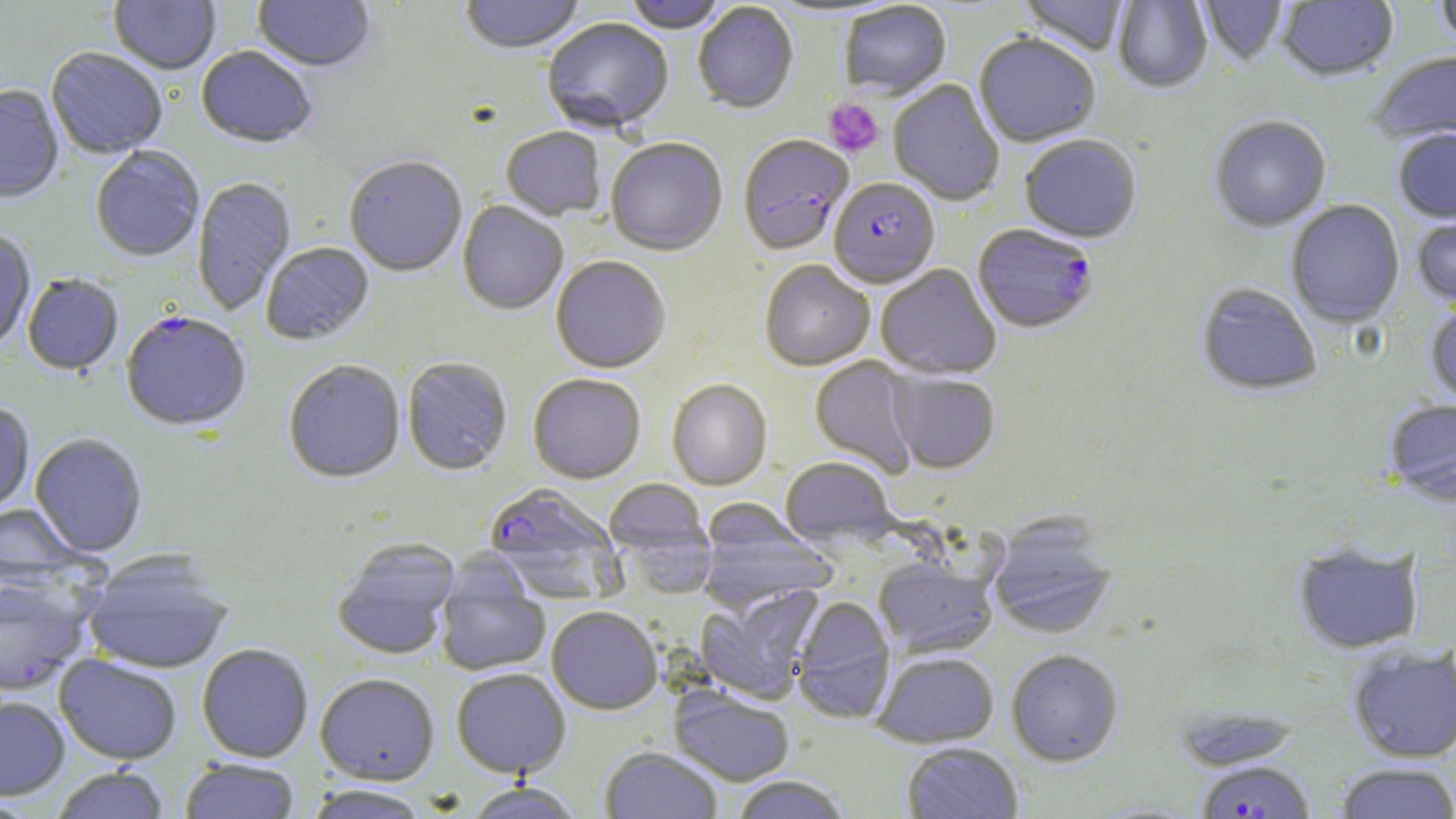
slide-level diagnosis = Plasmodium falciparum
preparation = thin blood smear
modality = light microscopy
field of view = one of a larger specimen
stain = May-Grünwald-Giemsa
image size = 1456×819 pixels
Plasmodium falciparum-infected red blood cell locations = approximate bounding boxes as [x1, y1, x2, y2] in pixels: [737, 136, 853, 256], [829, 179, 940, 290], [973, 225, 1098, 336], [121, 313, 251, 433], [484, 483, 622, 602], [1195, 759, 1317, 819]
platelet locations = approximate bounding boxes as [x1, y1, x2, y2] in pixels: [824, 98, 884, 158]
uninfected red blood cell locations = approximate bounding boxes as [x1, y1, x2, y2] in pixels: [109, 0, 221, 75], [253, 0, 375, 75], [460, 0, 585, 57], [623, 0, 728, 35], [1018, 0, 1130, 58], [1434, 0, 1456, 52], [1113, 1, 1212, 94], [1198, 1, 1288, 67], [1277, 1, 1398, 84], [692, 2, 799, 115], [839, 3, 951, 100], [543, 20, 674, 135], [974, 36, 1101, 149], [196, 48, 316, 150], [46, 49, 167, 160], [1369, 52, 1456, 148], [889, 80, 1005, 206], [0, 86, 64, 205], [1210, 117, 1331, 233], [500, 129, 606, 221], [1393, 130, 1456, 224], [1019, 136, 1142, 244], [606, 139, 727, 257], [91, 147, 205, 263], [344, 158, 467, 278], [192, 177, 297, 316], [1286, 201, 1405, 328], [457, 202, 568, 316], [1412, 212, 1456, 310], [0, 230, 36, 352], [261, 243, 374, 346], [551, 257, 671, 374], [759, 260, 875, 372], [876, 265, 1001, 380], [22, 275, 123, 377], [1196, 284, 1322, 397], [1425, 301, 1456, 409], [809, 356, 921, 479], [402, 357, 512, 476], [283, 361, 405, 485], [888, 371, 1001, 474], [528, 374, 646, 484], [666, 379, 773, 491], [1383, 399, 1456, 507], [0, 402, 35, 515], [29, 434, 147, 558], [780, 457, 898, 548], [603, 478, 712, 573], [0, 503, 88, 590], [697, 504, 837, 611], [988, 520, 1116, 640], [331, 538, 460, 660], [1293, 542, 1424, 654], [84, 554, 233, 674], [435, 556, 551, 676], [873, 557, 997, 657], [0, 578, 92, 696], [695, 585, 825, 704], [792, 596, 895, 725], [546, 606, 663, 715], [197, 644, 314, 763], [1347, 645, 1456, 763], [1006, 649, 1123, 766], [873, 651, 999, 748], [54, 655, 182, 765], [451, 669, 571, 779], [315, 674, 440, 786], [669, 686, 795, 786], [0, 696, 70, 801], [902, 742, 1024, 818], [599, 746, 723, 819], [179, 759, 300, 819], [1335, 763, 1456, 819], [52, 767, 169, 818], [729, 776, 852, 819], [462, 783, 583, 818], [304, 786, 430, 818], [0, 796, 45, 818]
magnification = 1000x